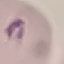

malaria_status: parasitized
capture: smartphone camera at the microscope eyepiece
image_type: automatically extracted cell patch, resized to 64 × 64 pixels
stain: Giemsa
preparation: thin smear